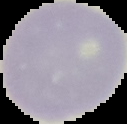
Summary:
  - Image size: 127×124 pixels
  - Image type: segmented cell region with the area outside set to black
  - Preparation: thin blood film
  - Result: no malaria parasites detected